Locate every Plasmodium parasite.
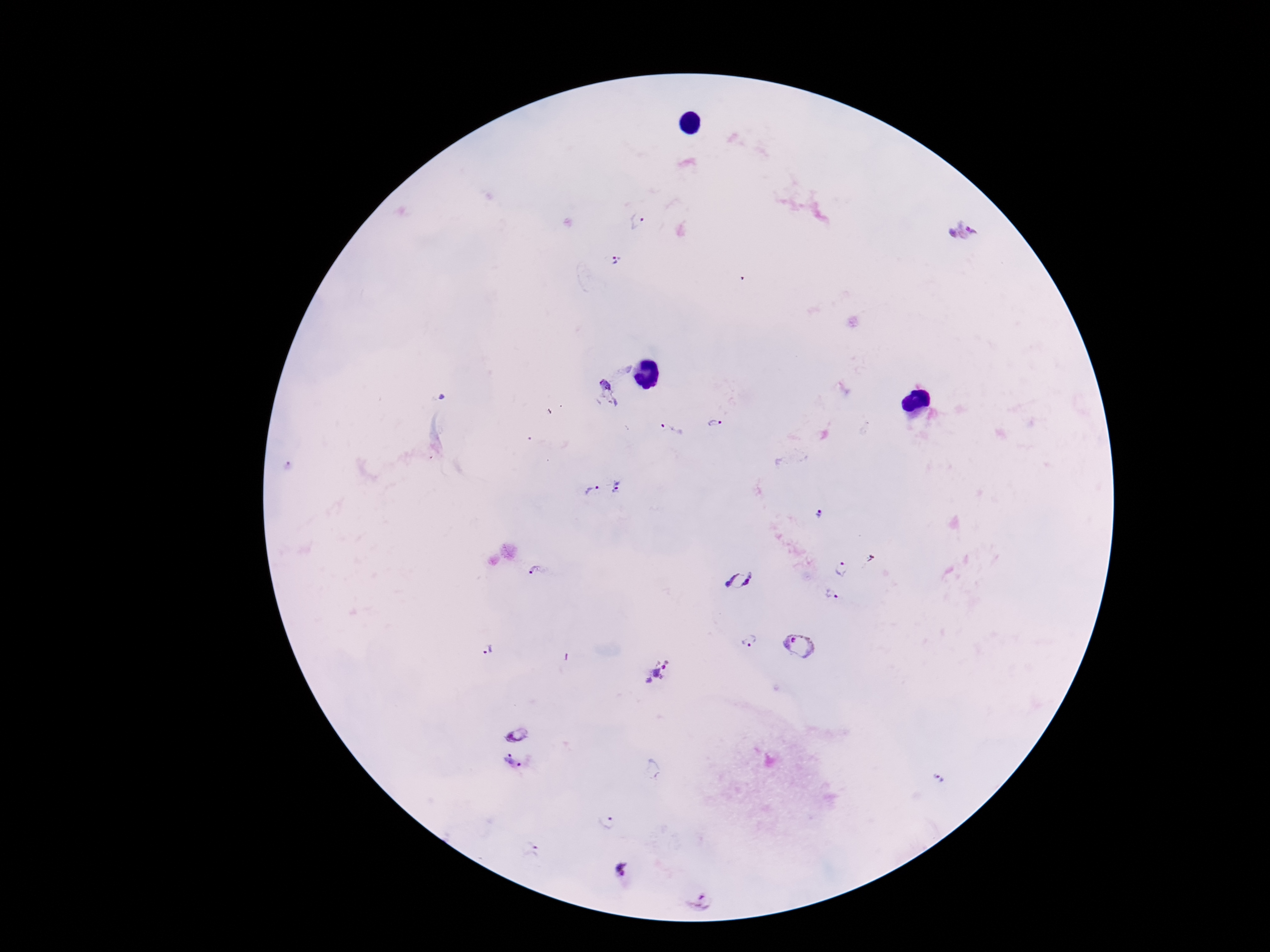
Approximate object centers, in pixels from the top-left corner.
Plasmodium parasites: (x=638, y=219), (x=963, y=234), (x=618, y=259), (x=608, y=391), (x=714, y=424), (x=670, y=431), (x=290, y=468), (x=617, y=487), (x=590, y=491), (x=819, y=516), (x=843, y=569), (x=536, y=572), (x=740, y=579), (x=832, y=593), (x=749, y=641), (x=798, y=645), (x=488, y=652), (x=657, y=673), (x=517, y=726), (x=511, y=771), (x=654, y=771), (x=937, y=780), (x=606, y=824), (x=531, y=849), (x=625, y=871), (x=699, y=902).

Summary:
  - Preparation: thick peripheral-blood smear
  - Stain: Giemsa
  - Capture: smartphone camera through the microscope eyepiece
  - Patient malaria status: positive
  - Image size: 1270×952 pixels
  - Field of view: single
  - Magnification: 100x